Assess this cell for malaria.
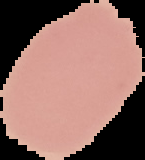

Uninfected.

Image is 145×160 pixels. The area outside the segmented cell region is set to black. From a thin blood film.